Report the malaria status of this cell.
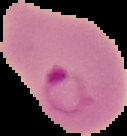

It is parasitized.

Summary:
  - Image type: segmented cell region on a black background
  - Image size: 127×136 pixels
  - Preparation: thin blood film